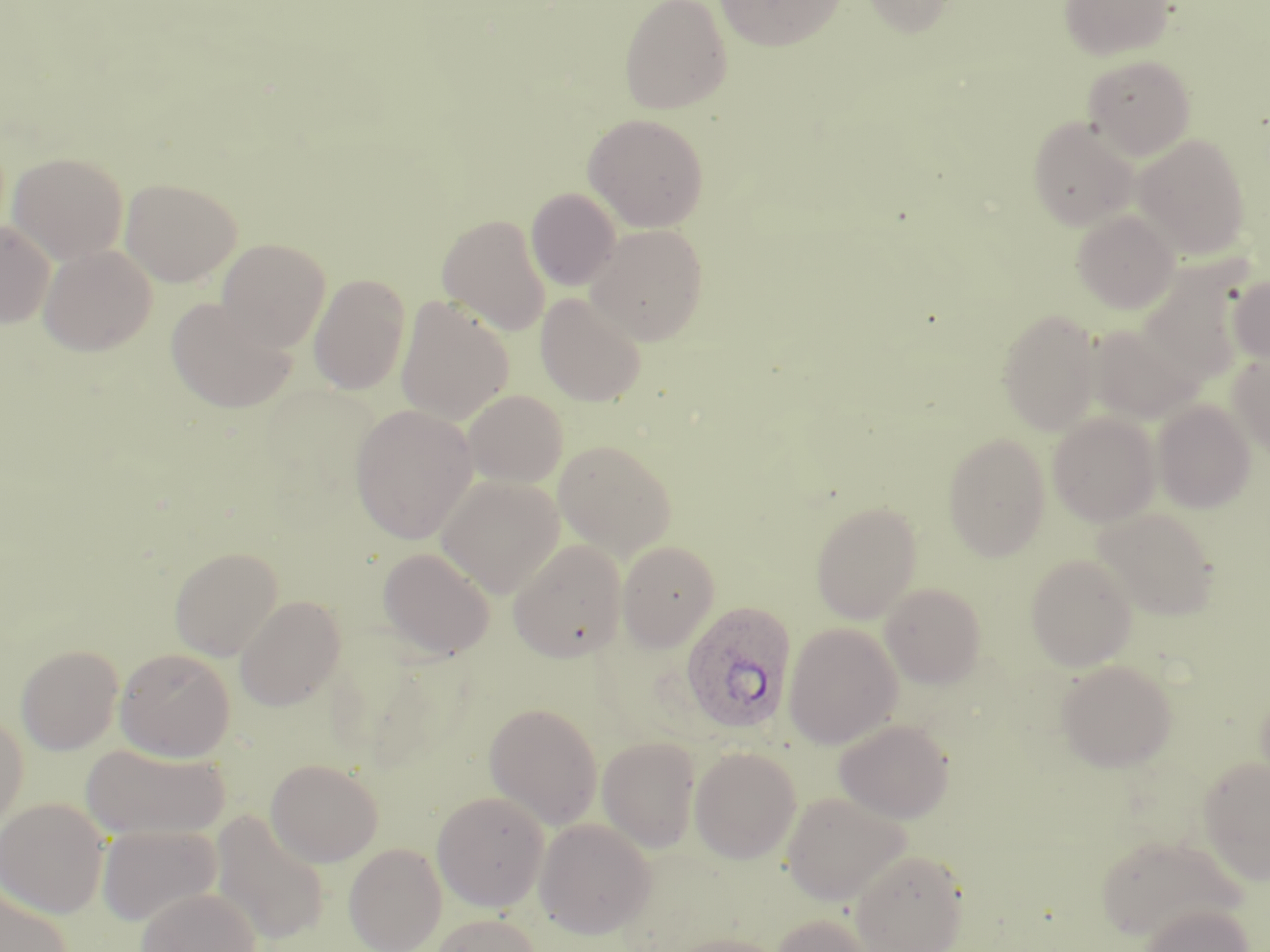

Summary:
  - Coordinate format: approximate bounding boxes as [x1, y1, x2, y2] in pixels
  - Uninfected red blood cell locations: [619, 0, 732, 115], [715, 0, 844, 50], [861, 0, 961, 36], [1059, 0, 1175, 61], [1083, 55, 1196, 159], [583, 113, 709, 232], [1028, 116, 1140, 230], [1133, 133, 1251, 259], [7, 151, 129, 263], [120, 177, 242, 286], [526, 188, 621, 291], [1071, 210, 1180, 313], [436, 213, 551, 335], [0, 220, 55, 329], [585, 223, 708, 345], [216, 238, 331, 351], [38, 244, 157, 356], [1136, 257, 1256, 390], [308, 274, 411, 395], [1229, 274, 1270, 365], [536, 292, 647, 407], [165, 296, 298, 414], [395, 296, 514, 425], [997, 307, 1102, 435], [1086, 324, 1197, 421], [1229, 352, 1270, 456], [462, 389, 568, 488], [1153, 400, 1256, 513], [350, 404, 478, 544], [1048, 413, 1160, 526], [942, 433, 1050, 561], [554, 440, 676, 559], [435, 474, 565, 597], [810, 501, 922, 623], [1092, 507, 1220, 620], [508, 539, 626, 662], [617, 540, 719, 651], [169, 546, 283, 660], [378, 546, 495, 660], [1025, 553, 1138, 671], [880, 583, 987, 688], [235, 595, 346, 711], [783, 622, 902, 749], [15, 644, 124, 755], [114, 647, 236, 761], [1056, 658, 1178, 772], [484, 702, 603, 830], [0, 711, 29, 832], [834, 718, 954, 823], [597, 736, 700, 854], [81, 743, 228, 840], [689, 746, 802, 864], [1198, 757, 1270, 884], [265, 758, 384, 867], [431, 791, 550, 911], [782, 791, 910, 906], [0, 798, 109, 917], [210, 810, 330, 946], [535, 818, 656, 938], [97, 824, 221, 926], [1094, 833, 1245, 941], [344, 843, 447, 951], [850, 847, 969, 952], [0, 887, 75, 952], [136, 887, 261, 952], [1140, 902, 1254, 952], [770, 912, 876, 952], [429, 913, 543, 952], [660, 933, 790, 952]
  - Plasmodium ovale-infected red blood cell locations: [680, 600, 796, 735]
  - Slide-level diagnosis: Plasmodium ovale
  - Image size: 1270×952 pixels
  - Field of view: single
  - Stain: May-Grünwald-Giemsa
  - Modality: light microscopy
  - Preparation: thin blood film
  - Magnification: 1000x